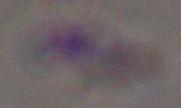

magnification = 1000x
modality = micrograph
identification = Toxoplasma gondii